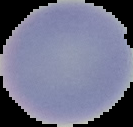

image size = 133×127 pixels
malaria status = uninfected
image type = cell region segmented out of the field of view; surrounding area masked to black
preparation = thin blood smear